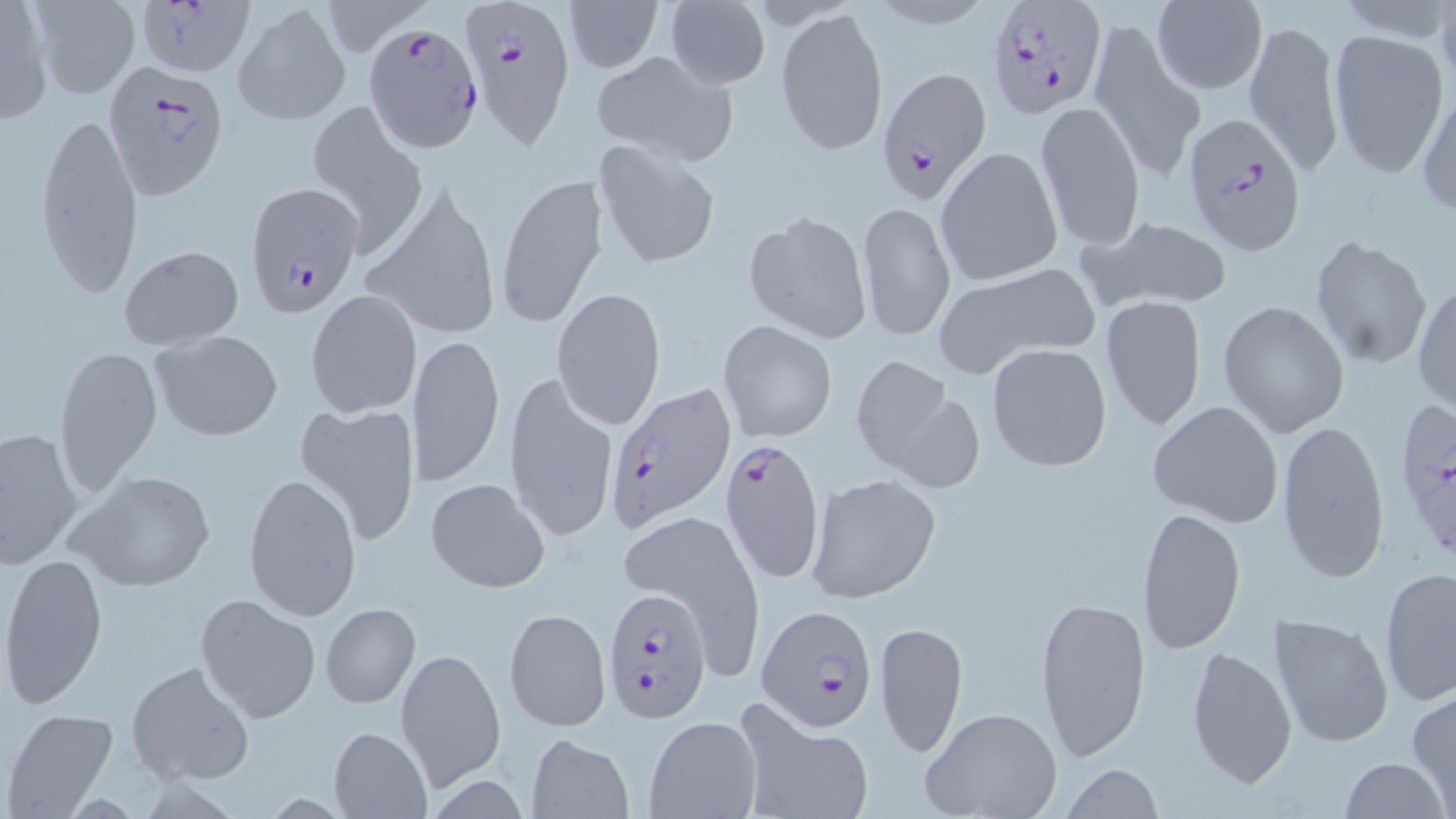

Summary:
  - Coordinate format: approximate bounding boxes as [x1, y1, x2, y2] in pixels
  - Uninfected red blood cell locations: [0, 0, 52, 124], [27, 0, 142, 99], [562, 1, 664, 75], [1152, 1, 1268, 95], [662, 2, 770, 89], [233, 3, 351, 126], [775, 7, 888, 157], [1243, 15, 1343, 174], [1088, 17, 1203, 179], [1330, 29, 1449, 180], [593, 51, 737, 165], [1415, 83, 1455, 221], [1033, 99, 1146, 250], [305, 100, 427, 250], [35, 110, 144, 298], [592, 139, 722, 271], [935, 146, 1063, 288], [494, 171, 611, 331], [360, 185, 502, 343], [857, 201, 956, 342], [743, 209, 873, 344], [1077, 214, 1237, 314], [1309, 234, 1432, 370], [118, 245, 246, 350], [933, 263, 1098, 377], [1413, 281, 1455, 413], [552, 287, 667, 433], [304, 289, 422, 419], [1100, 294, 1207, 431], [1217, 300, 1350, 436], [718, 320, 837, 442], [148, 328, 282, 441], [409, 333, 504, 486], [986, 342, 1114, 473], [53, 343, 163, 495], [849, 355, 962, 479], [503, 372, 618, 543], [1146, 400, 1284, 527], [295, 402, 422, 547], [1276, 420, 1391, 586], [1, 427, 84, 567], [64, 467, 216, 594], [242, 471, 362, 623], [805, 473, 942, 605], [426, 478, 550, 593], [621, 506, 765, 674], [1137, 507, 1247, 655], [2, 551, 109, 711], [1377, 565, 1456, 707], [1033, 591, 1152, 764], [195, 594, 322, 724], [320, 602, 420, 709], [504, 607, 611, 732], [1267, 611, 1396, 749], [875, 620, 969, 758], [1185, 644, 1299, 791], [394, 648, 505, 790], [126, 659, 256, 787], [1407, 689, 1455, 810], [734, 699, 875, 819], [920, 707, 1063, 819], [4, 708, 119, 817], [644, 715, 761, 818], [328, 726, 433, 817], [526, 734, 634, 818], [1340, 758, 1450, 818], [1060, 763, 1162, 819]
  - Plasmodium falciparum-infected red blood cell locations: [132, 0, 255, 79], [458, 0, 575, 149], [985, 0, 1109, 118], [363, 20, 485, 154], [102, 61, 226, 199], [876, 65, 993, 201], [1179, 113, 1309, 255], [244, 184, 364, 318], [606, 383, 736, 529], [1398, 405, 1455, 552], [721, 436, 827, 583], [604, 587, 712, 724], [756, 605, 876, 734]
  - Slide-level diagnosis: Plasmodium falciparum
  - Stain: May-Grünwald-Giemsa
  - Preparation: thin blood smear
  - Modality: light microscopy
  - Image size: 1456×819 pixels
  - Magnification: 1000x
  - Field of view: one of a larger specimen